Locate every blood parasite and identify its species.
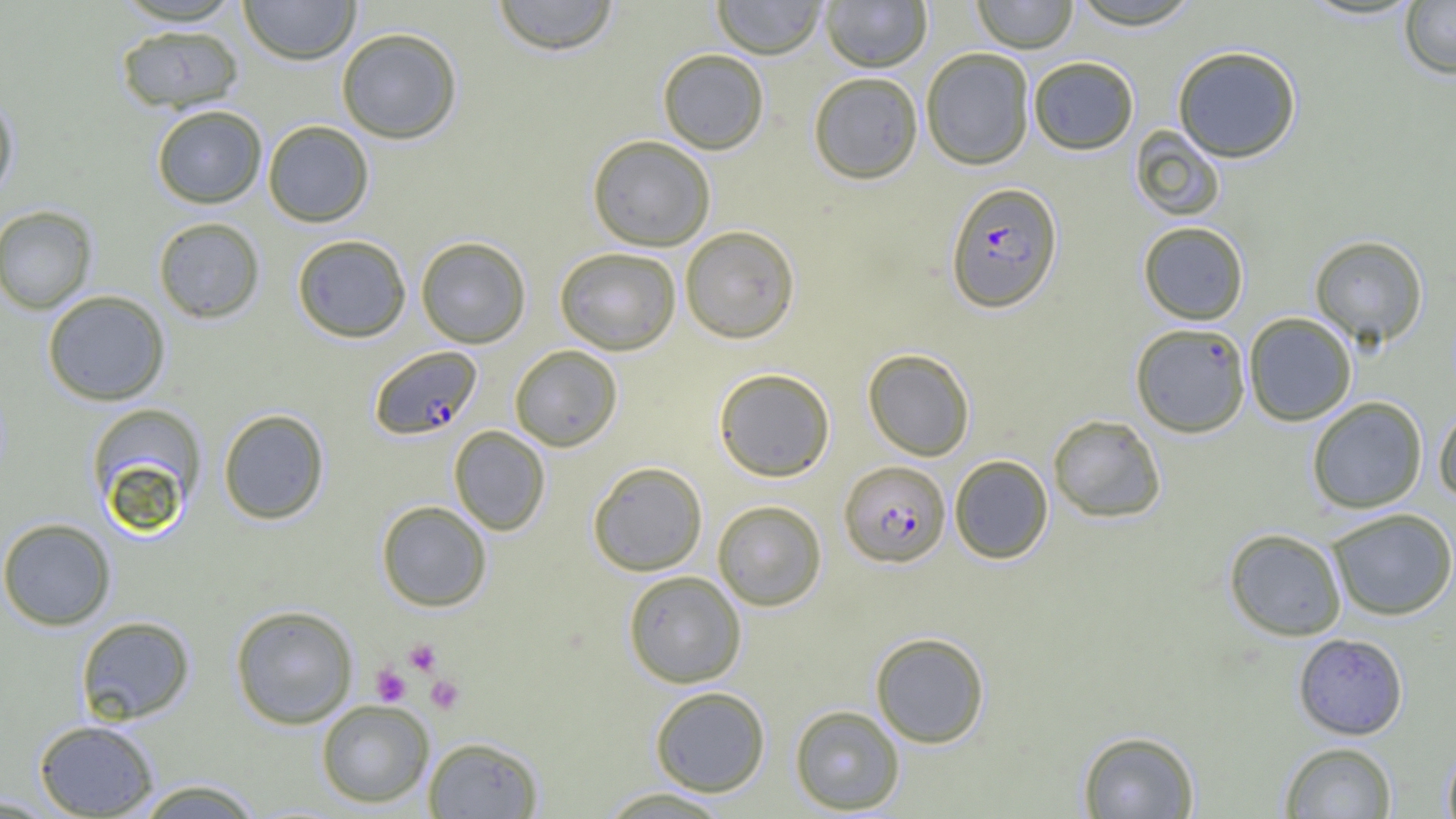
Approximate bounding boxes as (x1, y1, x2, y2) in pixels.
Plasmodium falciparum-infected red blood cells: (945, 181, 1063, 313), (1131, 323, 1251, 437), (369, 345, 482, 440), (840, 460, 950, 566).
No Plasmodium ovale, Plasmodium malariae, Plasmodium vivax, Babesia divergens, or Trypanosoma brucei observed.

Summary:
  - Uninfected red blood cell locations: (111, 0, 246, 26), (239, 0, 360, 65), (490, 0, 620, 55), (712, 0, 827, 59), (820, 0, 933, 73), (971, 0, 1078, 53), (1066, 0, 1204, 30), (1399, 1, 1456, 79), (115, 25, 244, 114), (336, 27, 463, 144), (1172, 45, 1302, 163), (921, 47, 1035, 169), (657, 48, 769, 154), (1028, 55, 1139, 155), (808, 71, 923, 184), (0, 92, 19, 204), (152, 104, 267, 208), (263, 120, 374, 227), (1130, 126, 1225, 221), (587, 134, 716, 251), (0, 205, 98, 314), (152, 217, 265, 324), (1138, 221, 1249, 325), (679, 225, 800, 343), (291, 234, 412, 342), (1309, 234, 1428, 347), (415, 236, 531, 348), (554, 247, 682, 356), (42, 290, 170, 406), (1243, 312, 1357, 426), (509, 345, 623, 451), (863, 348, 975, 461), (713, 367, 835, 482), (1306, 396, 1428, 514), (86, 402, 208, 532), (1433, 407, 1456, 503), (218, 408, 330, 525), (1048, 414, 1166, 523), (449, 426, 550, 536), (949, 455, 1054, 564), (588, 461, 708, 576), (712, 500, 827, 611), (376, 501, 491, 611), (1326, 508, 1455, 621), (0, 517, 117, 630), (1224, 528, 1347, 641), (623, 570, 746, 688), (230, 604, 358, 729), (75, 616, 195, 725), (870, 631, 990, 748), (1293, 633, 1409, 740), (649, 686, 771, 796), (316, 699, 434, 808), (790, 705, 905, 814), (33, 719, 159, 818), (1077, 729, 1200, 818), (422, 736, 544, 818), (1279, 741, 1397, 818), (1442, 742, 1456, 819), (132, 778, 264, 819), (596, 786, 735, 818), (0, 794, 61, 817)
  - Platelet locations: (403, 639, 442, 676), (371, 665, 411, 706), (425, 674, 465, 714)
  - Slide-level diagnosis: Plasmodium falciparum
  - Magnification: 1000x
  - Preparation: thin blood film
  - Field of view: one of a larger specimen
  - Modality: optical microscopy
  - Image size: 1456×819 pixels